Identify the blood parasite species.
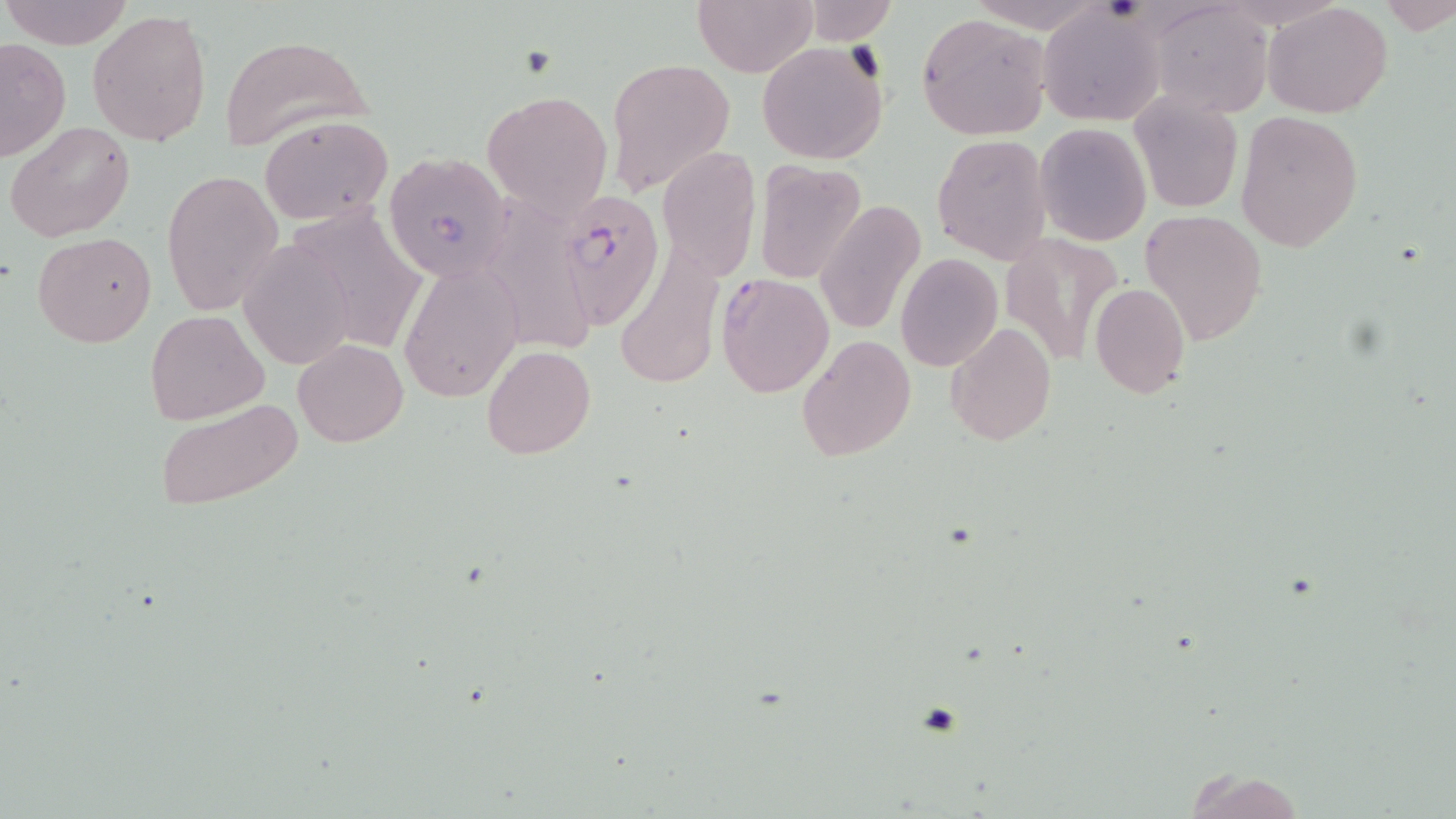
Plasmodium falciparum.

Summary:
  - Coordinate format: approximate bounding boxes as (x1, y1, x2, y2) in pixels
  - Plasmodium falciparum-infected red blood cell locations: (556, 189, 666, 326), (716, 272, 835, 396)
  - Platelet locations: (916, 703, 963, 738)
  - Uninfected red blood cell locations: (3, 0, 132, 50), (692, 0, 815, 76), (1381, 1, 1454, 37), (798, 2, 900, 44), (1148, 2, 1274, 119), (1263, 2, 1392, 118), (87, 8, 212, 148), (917, 11, 1053, 141), (1041, 11, 1165, 125), (217, 32, 377, 152), (0, 38, 71, 162), (757, 42, 889, 164), (605, 58, 735, 196), (483, 89, 612, 219), (1128, 91, 1243, 215), (1235, 109, 1364, 252), (258, 114, 394, 225), (5, 121, 135, 243), (1034, 122, 1153, 247), (932, 134, 1051, 264), (657, 145, 761, 279), (381, 151, 513, 283), (753, 158, 867, 284), (161, 168, 285, 315), (493, 188, 595, 359), (814, 200, 926, 336), (1141, 208, 1267, 345), (1000, 231, 1125, 368), (34, 232, 156, 348), (238, 239, 358, 370), (896, 253, 1003, 372), (398, 258, 523, 403), (1090, 283, 1190, 399), (145, 309, 269, 425), (945, 322, 1056, 446), (798, 333, 916, 461), (293, 339, 408, 447), (481, 344, 595, 459), (152, 395, 303, 514), (1183, 770, 1307, 819)
  - Field of view: one of a larger specimen
  - Image size: 1456×819 pixels
  - Magnification: 1000x
  - Modality: optical microscopy
  - Preparation: thin blood film
  - Stain: May-Grünwald-Giemsa